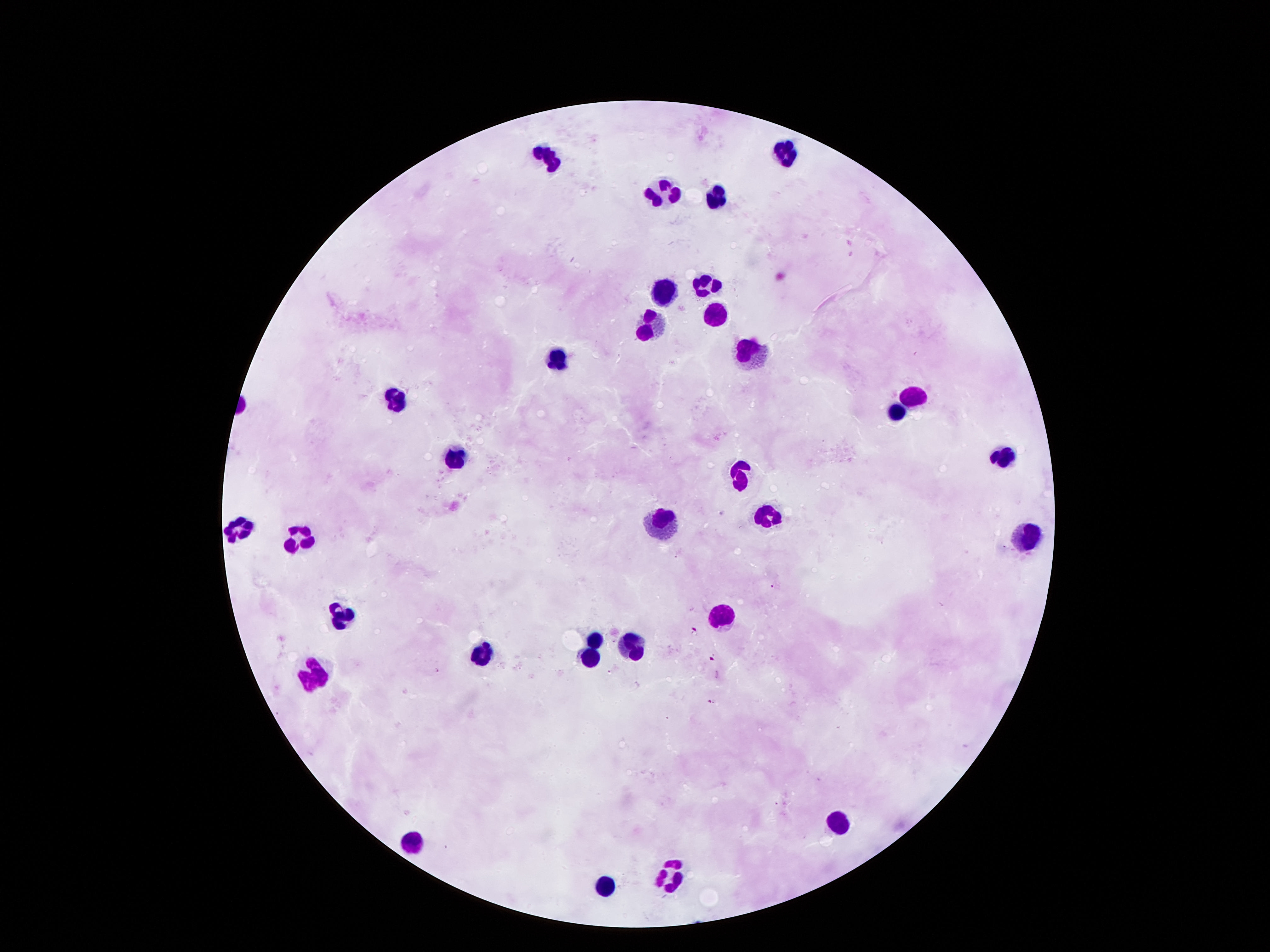

magnification = 100x
capture = smartphone camera through the microscope eyepiece
stain = Giemsa
field of view = single
patient malaria status = uninfected
preparation = thick blood film
image size = 1270×952 pixels
leukocyte locations = approximate centers as [x, y] in pixels: [547, 157], [786, 157], [661, 183], [715, 195], [707, 279], [663, 293], [714, 317], [649, 326], [747, 349], [560, 361], [911, 393], [398, 394], [895, 414], [1004, 455], [455, 456], [742, 469], [765, 511], [661, 527], [238, 529], [1025, 536], [296, 537], [343, 610], [723, 614], [596, 641], [632, 643], [486, 654], [588, 656], [316, 672], [839, 815], [412, 838], [673, 873], [603, 883]